State which parasite is depicted.
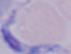
A trypanosome.

modality = photomicrograph
magnification = 1000x